Draw a bounding box around every leukocyte (white blood cell).
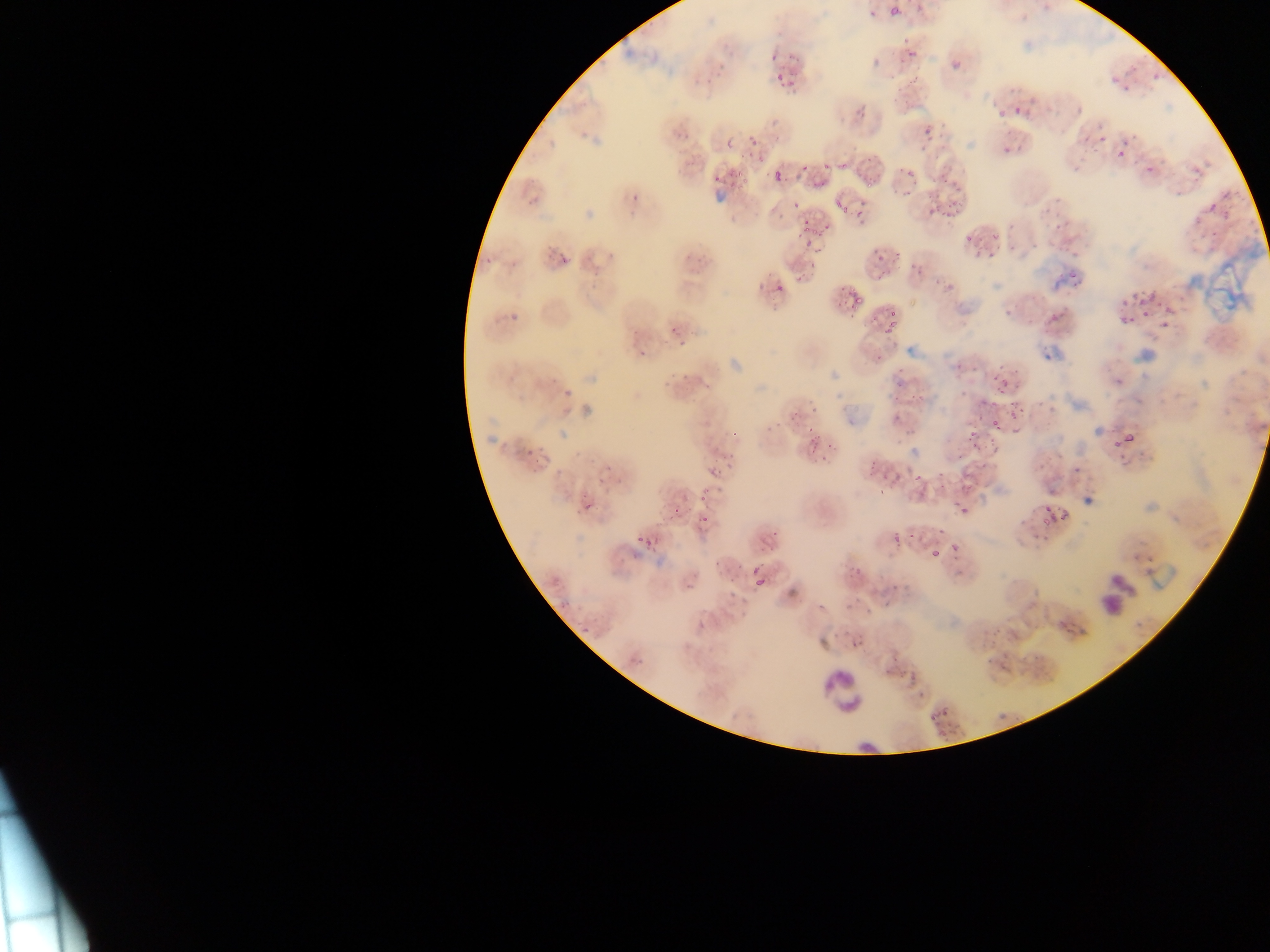
Approximate bounding boxes as [left, top, right, bottom] in pixels.
Leukocytes: [1095, 572, 1130, 613], [815, 662, 869, 724].

{
  "capture": "mobile-phone photograph through a microscope",
  "preparation": "thin blood smear",
  "image_size": "1270×952 pixels",
  "plasmodium_parasite_locations": "approximate bounding boxes as [left, top, right, bottom] in pixels: [886, 4, 904, 22], [865, 7, 878, 21], [898, 42, 915, 67], [869, 56, 883, 69], [949, 57, 965, 73], [770, 62, 791, 83], [1145, 63, 1167, 79], [1116, 66, 1140, 98], [904, 94, 921, 110], [1069, 95, 1089, 115], [998, 99, 1027, 119], [850, 102, 868, 122], [723, 130, 743, 145], [916, 130, 931, 150], [1079, 130, 1093, 148], [746, 131, 760, 149], [999, 134, 1024, 158], [1102, 134, 1131, 163], [1141, 144, 1165, 179], [712, 154, 741, 185], [1063, 156, 1084, 182], [795, 157, 805, 179], [822, 158, 835, 172], [900, 165, 918, 183], [773, 171, 784, 183], [812, 175, 826, 192], [941, 181, 952, 191], [923, 191, 937, 201], [1203, 191, 1230, 221], [830, 192, 852, 218], [630, 193, 642, 206], [785, 193, 799, 207], [941, 201, 956, 215], [849, 203, 868, 227], [925, 210, 938, 234], [800, 222, 820, 242], [963, 225, 975, 239], [985, 227, 1001, 241], [1050, 228, 1067, 235], [870, 240, 888, 267], [1003, 243, 1021, 263], [968, 244, 988, 261], [550, 249, 568, 268], [507, 256, 518, 270], [909, 264, 926, 278], [1062, 267, 1086, 290], [757, 277, 766, 293], [790, 278, 810, 289], [771, 283, 785, 298], [943, 286, 956, 294], [1138, 286, 1154, 303], [1117, 288, 1137, 309], [842, 289, 859, 308], [878, 298, 892, 319], [502, 306, 516, 326], [1154, 309, 1178, 335], [1116, 310, 1137, 329], [1047, 311, 1064, 322], [879, 321, 899, 344], [668, 325, 686, 339], [676, 344, 686, 356], [634, 348, 646, 365], [872, 352, 885, 363], [992, 362, 1013, 383], [676, 364, 695, 378], [891, 364, 909, 393], [552, 381, 569, 404], [991, 383, 1005, 398], [913, 392, 935, 409], [963, 395, 985, 413], [807, 398, 818, 415], [1009, 398, 1026, 425], [891, 404, 907, 428], [991, 411, 1007, 438], [783, 416, 793, 431], [964, 421, 982, 453], [804, 424, 813, 438], [724, 427, 740, 438], [1111, 428, 1141, 456], [813, 439, 850, 461], [522, 444, 536, 458], [717, 451, 739, 461], [867, 455, 877, 473], [1068, 459, 1082, 473], [706, 464, 719, 478], [882, 467, 896, 485], [959, 469, 980, 488], [933, 479, 948, 492], [908, 483, 925, 506], [709, 487, 728, 500], [699, 494, 708, 502], [1038, 495, 1075, 533], [958, 500, 974, 516], [580, 502, 590, 513], [669, 506, 682, 518], [697, 511, 711, 527], [891, 526, 905, 545], [937, 526, 948, 537], [633, 528, 646, 546], [645, 538, 655, 549], [949, 538, 966, 548], [928, 546, 942, 560], [848, 550, 869, 584], [749, 570, 770, 593], [682, 575, 695, 591], [727, 578, 744, 600], [888, 582, 902, 593], [844, 586, 866, 612], [887, 601, 897, 611], [846, 622, 858, 644], [579, 624, 585, 633], [636, 657, 646, 671], [928, 706, 947, 725] | approximate [x, y] pixel centers of objects too small to bound: [1113, 81], [904, 192]",
  "field_of_view": "single",
  "country": "Ghana"
}